Describe the morphology of the red blood cells.
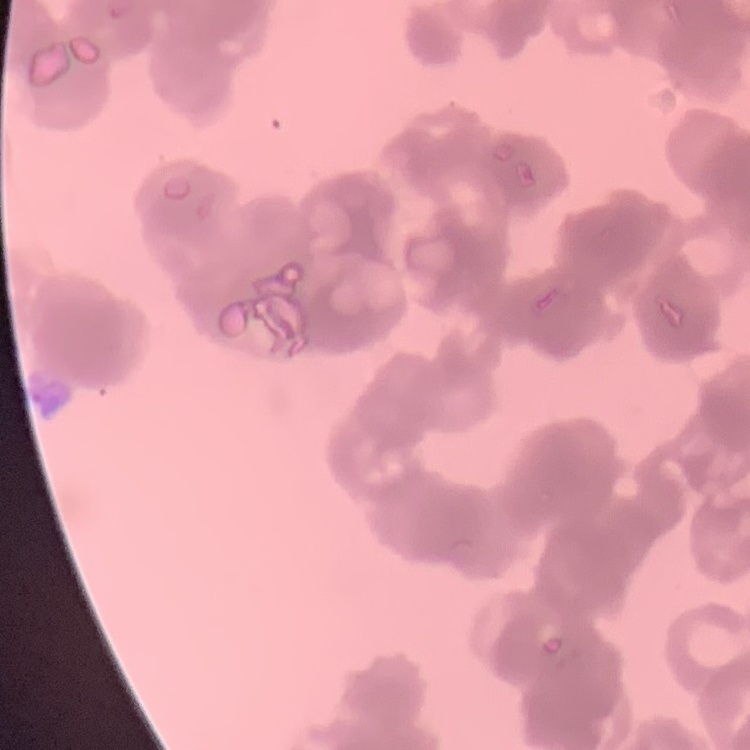
Rouleaux formation.

Thin peripheral smear. Square crop of a larger photomicrograph. Field's or Giemsa stain.